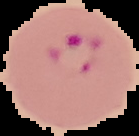

From a thin blood film. Result: Plasmodium parasites detected. The area outside the segmented cell region is set to black. Image is 139×136 pixels.